Give the position of every Plasmodium parasite.
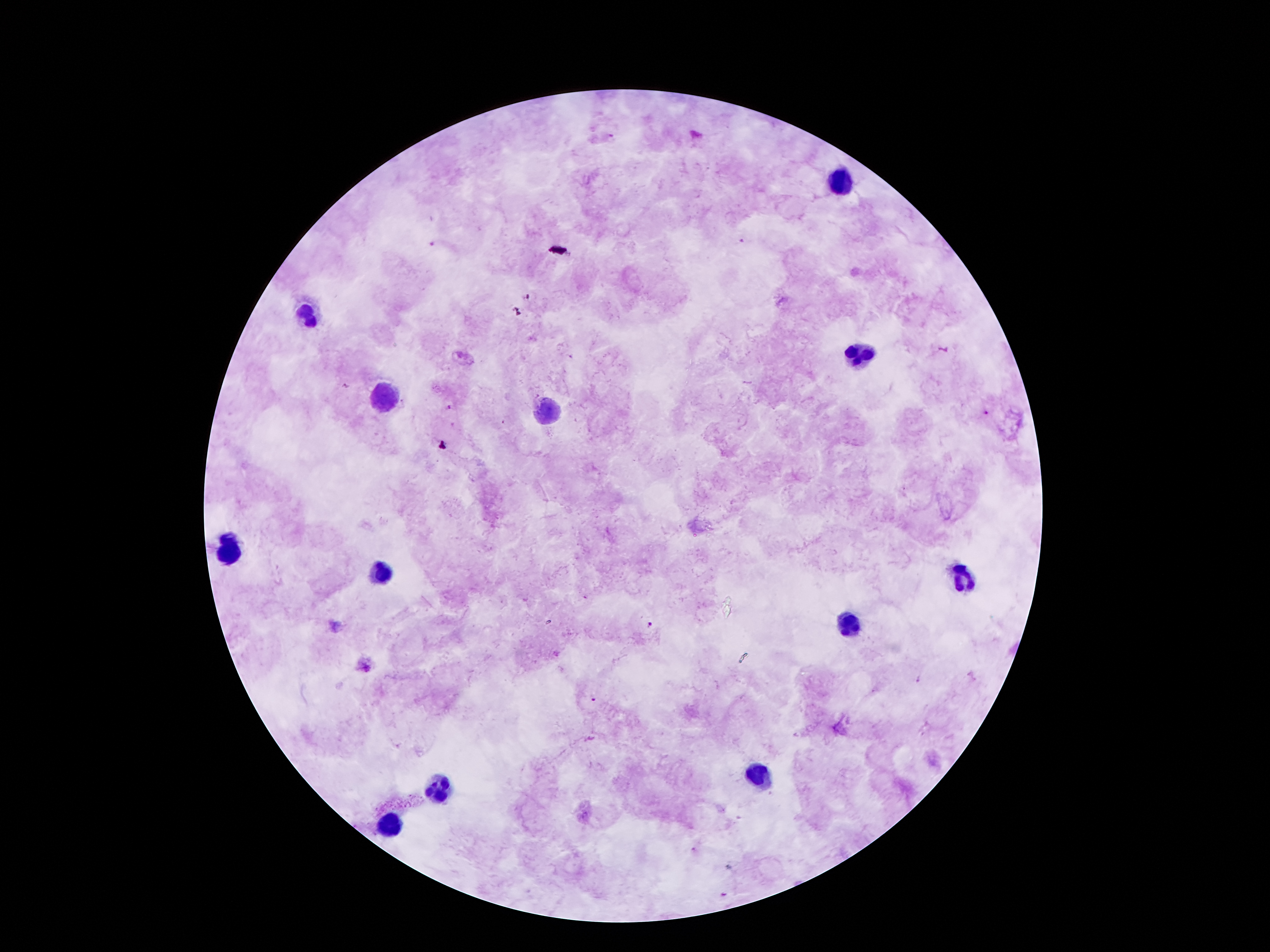

Approximate centers as (x, y) in pixels.
Plasmodium parasites: (611, 136), (742, 241), (430, 244), (528, 297), (450, 407), (986, 412), (651, 624), (594, 699), (694, 850), (724, 894).

Summary:
  - Leukocyte locations: (839, 181), (306, 316), (859, 358), (386, 398), (547, 409), (229, 550), (381, 575), (961, 577), (848, 626), (762, 776), (439, 789), (390, 827)
  - Preparation: thick blood smear
  - Magnification: 100x
  - Patient malaria status: positive for Plasmodium falciparum
  - Image size: 1270×952 pixels
  - Capture: smartphone camera through the microscope eyepiece
  - Stain: Giemsa
  - Field of view: one from this slide